Locate every blood parasite and identify its species.
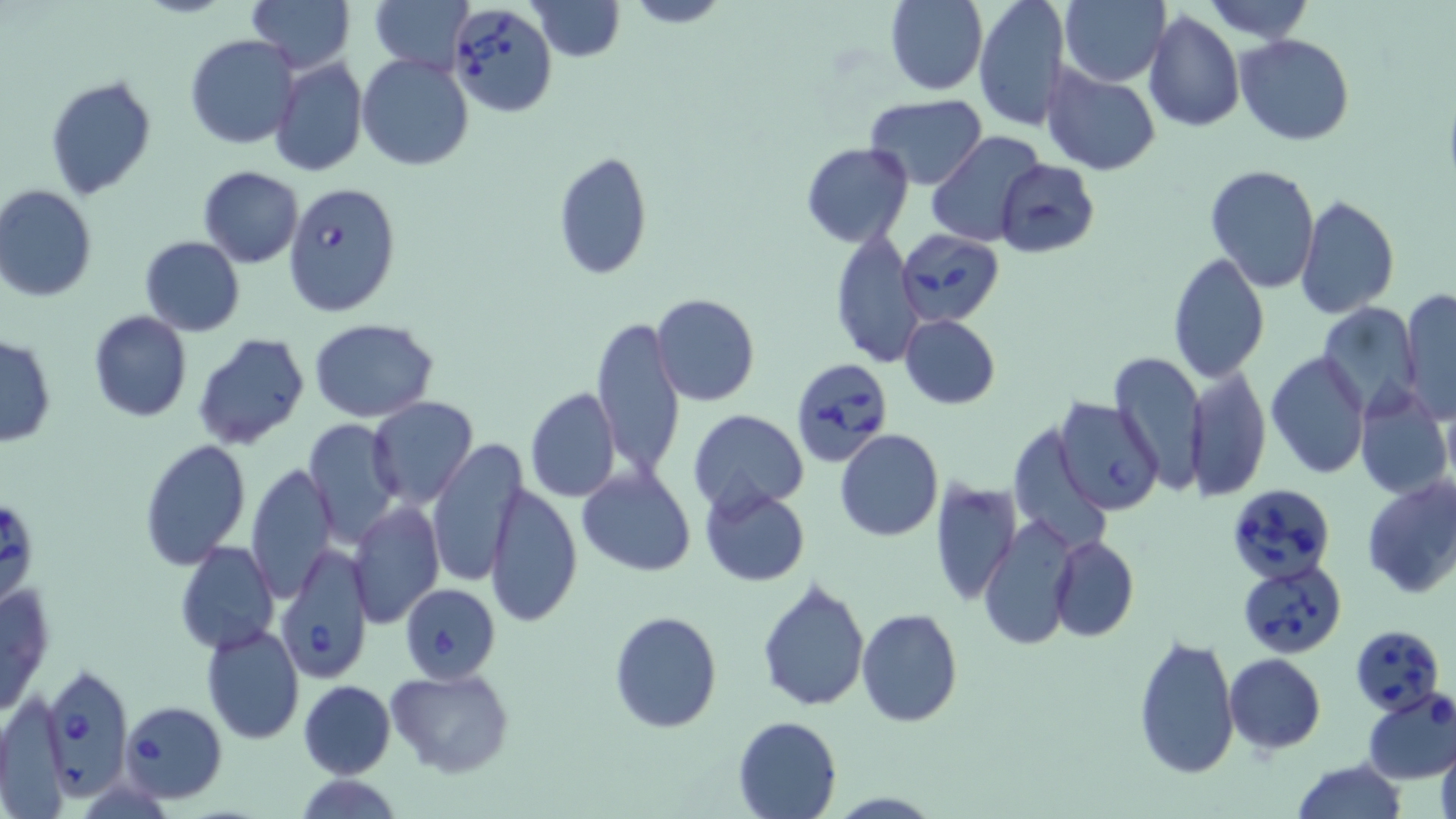

Approximate bounding boxes as named x1/y1/x2/y2 corners in pixels.
Babesia divergens-infected red blood cells: (x1=447, y1=3, x2=558, y2=117), (x1=283, y1=180, x2=403, y2=316), (x1=898, y1=232, x2=1006, y2=323), (x1=788, y1=357, x2=894, y2=468), (x1=1225, y1=481, x2=1336, y2=583), (x1=0, y1=503, x2=39, y2=604), (x1=275, y1=542, x2=374, y2=685), (x1=1237, y1=557, x2=1349, y2=658), (x1=399, y1=583, x2=500, y2=685), (x1=1350, y1=623, x2=1444, y2=714), (x1=41, y1=661, x2=133, y2=795), (x1=119, y1=701, x2=229, y2=802).
No Plasmodium falciparum, Plasmodium ovale, Plasmodium malariae, Plasmodium vivax, or Trypanosoma brucei observed.

Summary:
  - Uninfected red blood cell locations: (x1=250, y1=0, x2=352, y2=73), (x1=372, y1=0, x2=474, y2=75), (x1=527, y1=0, x2=626, y2=62), (x1=623, y1=0, x2=731, y2=28), (x1=884, y1=0, x2=989, y2=95), (x1=974, y1=0, x2=1070, y2=131), (x1=1060, y1=0, x2=1170, y2=87), (x1=1198, y1=0, x2=1316, y2=42), (x1=1142, y1=9, x2=1245, y2=132), (x1=1234, y1=34, x2=1356, y2=146), (x1=186, y1=35, x2=300, y2=150), (x1=358, y1=54, x2=473, y2=171), (x1=269, y1=56, x2=367, y2=179), (x1=1042, y1=64, x2=1161, y2=175), (x1=45, y1=74, x2=158, y2=201), (x1=865, y1=94, x2=986, y2=189), (x1=927, y1=131, x2=1045, y2=247), (x1=801, y1=141, x2=914, y2=247), (x1=552, y1=150, x2=654, y2=282), (x1=994, y1=159, x2=1100, y2=258), (x1=1204, y1=164, x2=1320, y2=292), (x1=198, y1=166, x2=302, y2=267), (x1=1, y1=185, x2=97, y2=303), (x1=1297, y1=194, x2=1400, y2=318), (x1=830, y1=226, x2=922, y2=370), (x1=140, y1=236, x2=245, y2=336), (x1=1167, y1=253, x2=1270, y2=384), (x1=1399, y1=289, x2=1455, y2=422), (x1=651, y1=293, x2=760, y2=406), (x1=1320, y1=303, x2=1422, y2=416), (x1=88, y1=310, x2=193, y2=423), (x1=899, y1=314, x2=1000, y2=409), (x1=591, y1=316, x2=685, y2=482), (x1=309, y1=319, x2=439, y2=420), (x1=192, y1=333, x2=310, y2=449), (x1=0, y1=334, x2=55, y2=448), (x1=1265, y1=351, x2=1371, y2=479), (x1=1110, y1=352, x2=1207, y2=490), (x1=1186, y1=365, x2=1272, y2=501), (x1=1353, y1=380, x2=1452, y2=502), (x1=523, y1=388, x2=621, y2=503), (x1=367, y1=397, x2=479, y2=510), (x1=1054, y1=398, x2=1167, y2=516), (x1=688, y1=409, x2=809, y2=514), (x1=388, y1=415, x2=509, y2=556), (x1=304, y1=419, x2=403, y2=546), (x1=835, y1=429, x2=944, y2=541), (x1=138, y1=437, x2=252, y2=570), (x1=426, y1=438, x2=527, y2=588), (x1=246, y1=461, x2=338, y2=603), (x1=577, y1=464, x2=696, y2=576), (x1=1359, y1=474, x2=1456, y2=601), (x1=929, y1=476, x2=1022, y2=608), (x1=484, y1=482, x2=582, y2=628), (x1=699, y1=485, x2=810, y2=587), (x1=348, y1=501, x2=445, y2=628), (x1=978, y1=516, x2=1077, y2=650), (x1=1049, y1=534, x2=1139, y2=641), (x1=176, y1=541, x2=278, y2=653), (x1=757, y1=575, x2=870, y2=712), (x1=1, y1=580, x2=54, y2=720), (x1=855, y1=607, x2=962, y2=726), (x1=609, y1=610, x2=722, y2=732), (x1=201, y1=624, x2=305, y2=744), (x1=1133, y1=634, x2=1241, y2=780), (x1=1224, y1=654, x2=1325, y2=753), (x1=385, y1=668, x2=515, y2=779), (x1=298, y1=680, x2=397, y2=779), (x1=1360, y1=689, x2=1456, y2=783), (x1=732, y1=715, x2=843, y2=819), (x1=1436, y1=740, x2=1456, y2=819), (x1=1291, y1=760, x2=1408, y2=819), (x1=294, y1=774, x2=407, y2=817)
  - Slide-level diagnosis: Babesia divergens
  - Field of view: one of a larger specimen
  - Image size: 1456×819 pixels
  - Preparation: thin blood smear
  - Modality: light microscopy
  - Stain: May-Grünwald-Giemsa
  - Magnification: 1000x